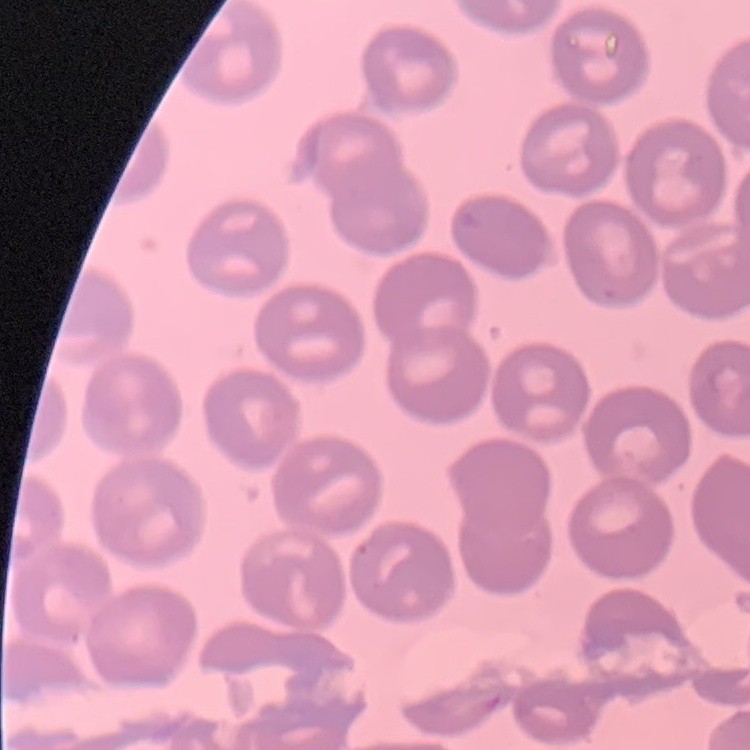

The erythrocytes exhibit no rouleaux formation. Square crop of a larger photomicrograph. Field's or Giemsa stain. Thin peripheral smear.